Name the parasite shown.
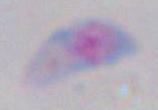
This is Toxoplasma gondii.

Summary:
  - Modality: micrograph
  - Magnification: 1000x